Report the malaria status of this cell.
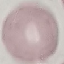

It is uninfected.

Automatically extracted cell patch, resized to 64 × 64 pixels. Giemsa stain. Acquired by smartphone through the microscope eyepiece. Thin smear of blood.